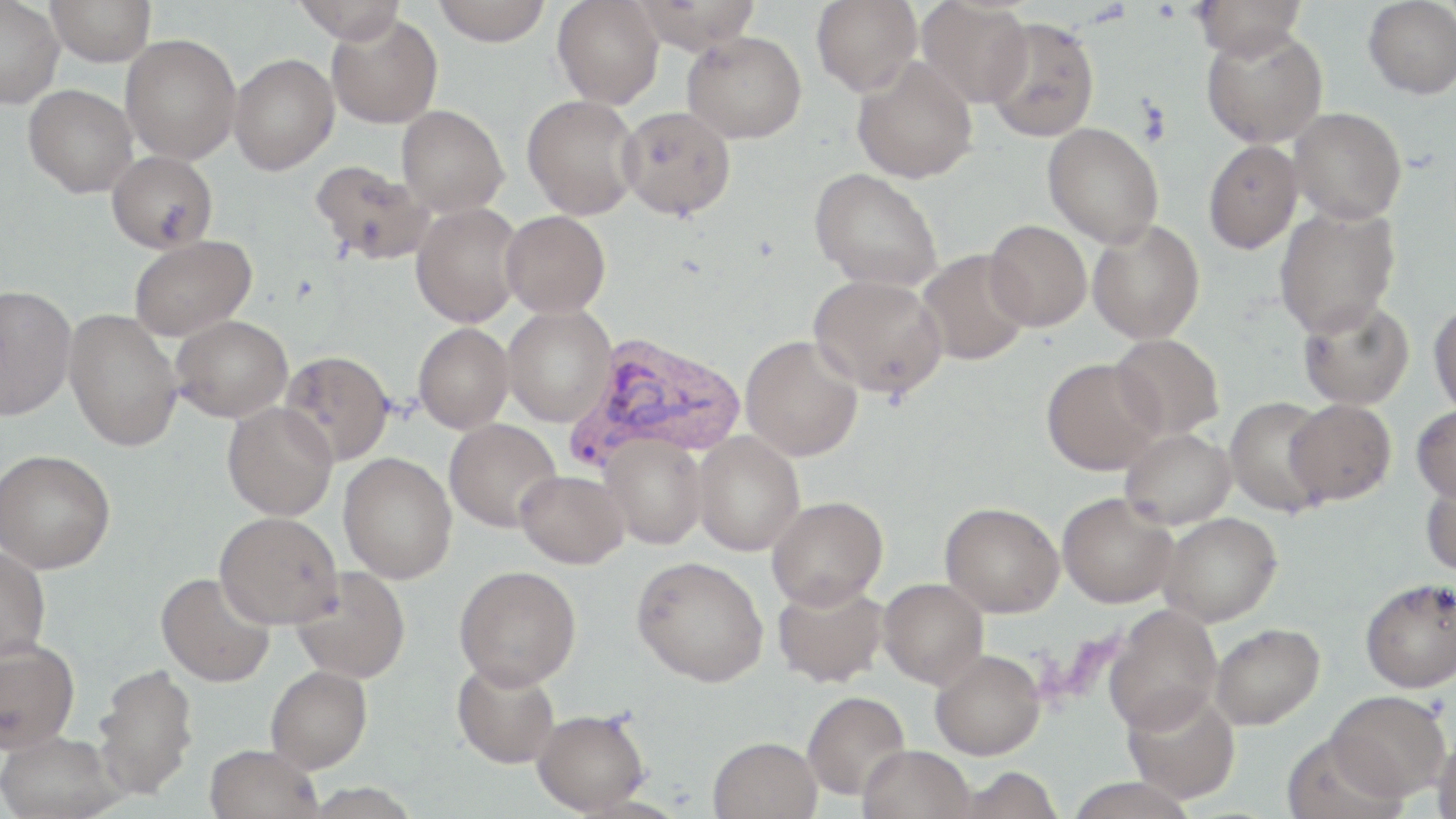
Plasmodium vivax-infected red blood cell locations = approximate bounding boxes as [x1, y1, x2, y2] in pixels: [565, 331, 746, 471]
slide-level diagnosis = Plasmodium vivax
preparation = thin blood film
image size = 1456×819 pixels
modality = optical microscopy
stain = May-Grünwald-Giemsa
field of view = single
magnification = 1000x
uninfected red blood cell locations = approximate bounding boxes as [x1, y1, x2, y2] in pixels: [0, 0, 63, 108], [47, 0, 155, 66], [292, 0, 408, 44], [431, 0, 553, 46], [552, 0, 664, 108], [631, 0, 762, 52], [812, 0, 921, 95], [1192, 0, 1307, 60], [1363, 0, 1456, 98], [917, 1, 1033, 108], [326, 14, 443, 128], [983, 16, 1100, 142], [1201, 27, 1328, 148], [682, 31, 807, 143], [121, 33, 241, 164], [229, 53, 339, 174], [851, 58, 978, 184], [23, 84, 137, 197], [522, 94, 642, 220], [396, 104, 509, 217], [617, 106, 736, 220], [1289, 107, 1406, 225], [1043, 122, 1165, 248], [1202, 140, 1302, 254], [106, 151, 217, 254], [309, 160, 434, 267], [809, 168, 943, 292], [411, 203, 523, 328], [1274, 206, 1400, 338], [501, 210, 610, 317], [984, 220, 1092, 331], [1088, 220, 1204, 344], [128, 234, 257, 341], [916, 248, 1032, 366], [809, 273, 947, 399], [0, 284, 77, 421], [1296, 297, 1415, 410], [1428, 300, 1456, 418], [502, 305, 616, 428], [64, 307, 183, 452], [171, 314, 293, 422], [413, 323, 514, 433], [1110, 333, 1225, 441], [740, 335, 863, 461], [279, 350, 395, 466], [1041, 357, 1164, 475], [1224, 397, 1333, 517], [1284, 399, 1396, 505], [222, 401, 337, 521], [1411, 405, 1456, 503], [444, 419, 562, 533], [1119, 428, 1235, 529], [692, 432, 805, 556], [601, 433, 707, 549], [1, 449, 116, 573], [338, 453, 456, 584], [516, 470, 629, 569], [1420, 475, 1456, 579], [1057, 492, 1178, 607], [767, 496, 887, 609], [940, 502, 1064, 617], [214, 511, 342, 629], [1158, 512, 1282, 627], [0, 546, 51, 663], [632, 555, 768, 686], [454, 565, 581, 690], [289, 566, 410, 682], [155, 571, 275, 688], [1360, 577, 1456, 693], [878, 578, 988, 689], [772, 579, 889, 688], [1104, 605, 1222, 734], [1210, 623, 1325, 730], [0, 638, 80, 753], [930, 650, 1045, 760], [451, 660, 560, 769], [91, 662, 199, 800], [265, 665, 372, 773], [1122, 690, 1240, 804], [1327, 690, 1451, 801], [802, 691, 910, 801], [531, 708, 650, 814], [0, 730, 125, 819], [1432, 732, 1456, 819], [707, 736, 822, 819], [203, 744, 323, 819], [858, 745, 974, 819]